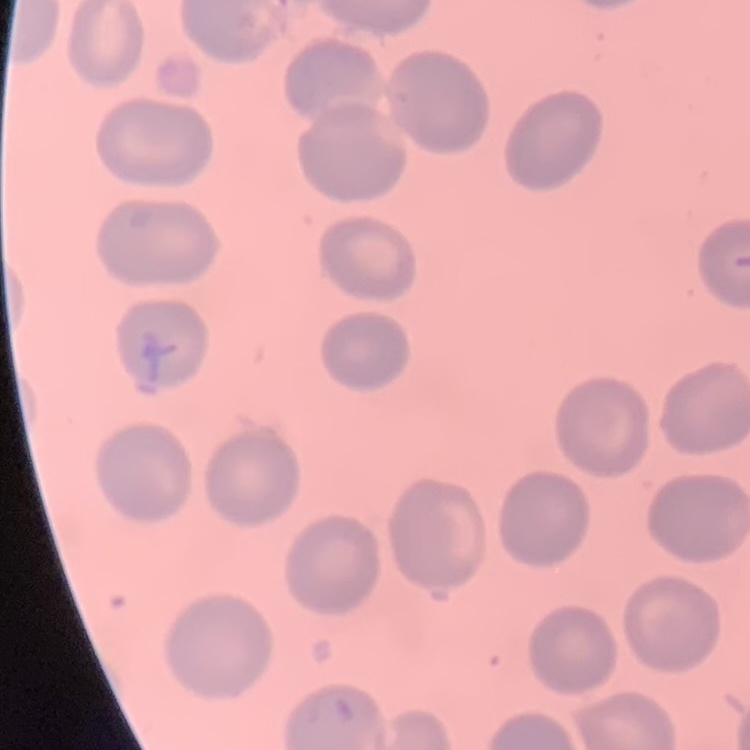

The erythrocytes show no rouleaux formation. Square crop of a larger photomicrograph. Field's or Giemsa stain. Thin peripheral smear.